Outline each blood parasite and name the species.
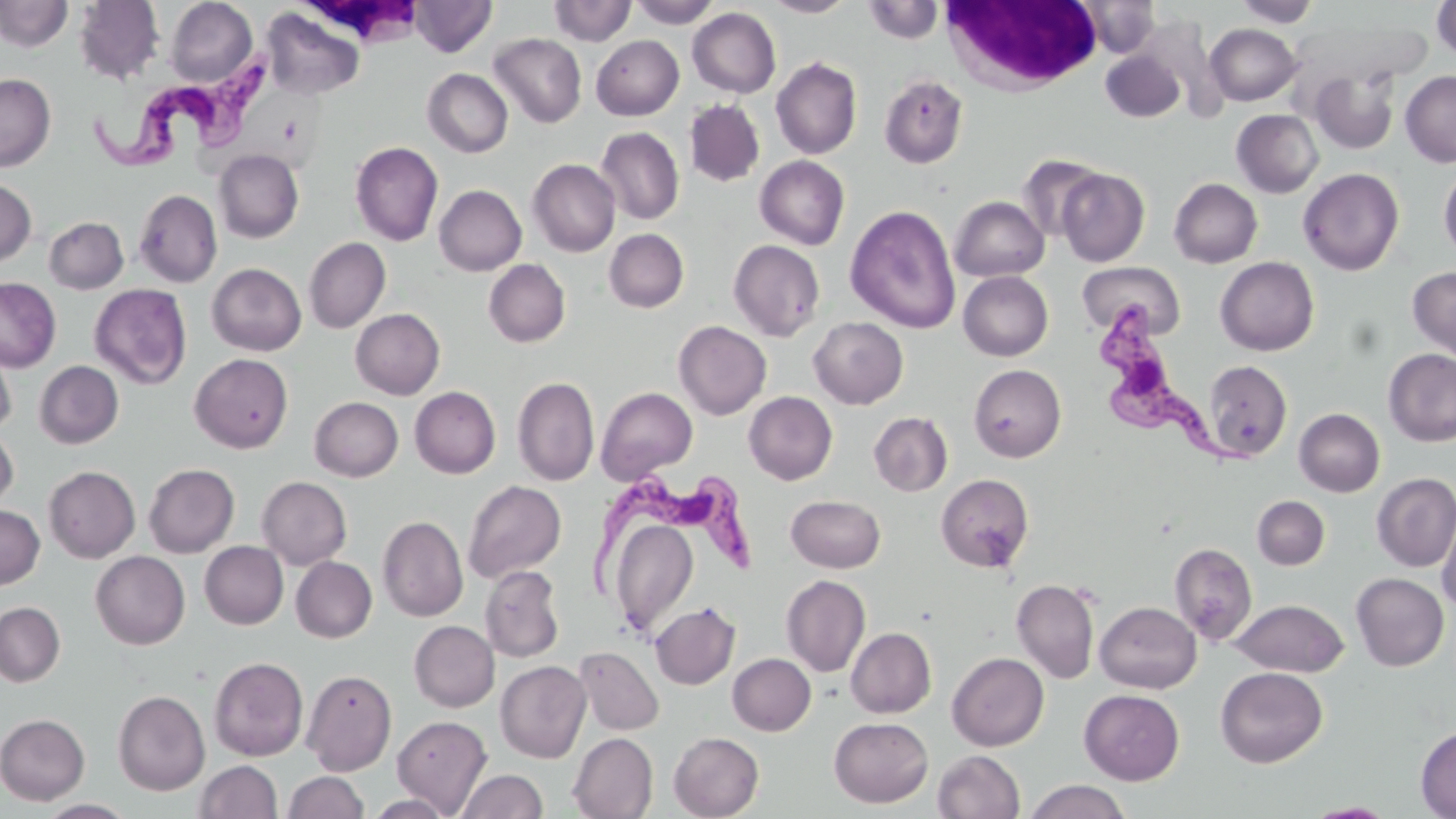

Approximate bounding boxes as named x1/y1/x2/y2 corners in pixels.
Trypanosoma brucei: (x1=91, y1=58, x2=277, y2=172), (x1=1099, y1=305, x2=1256, y2=478), (x1=589, y1=474, x2=756, y2=607).
No Plasmodium falciparum, Plasmodium ovale, Plasmodium malariae, Plasmodium vivax, or Babesia divergens observed.

Summary:
  - White blood cell locations: (x1=299, y1=0, x2=428, y2=50), (x1=941, y1=0, x2=1104, y2=95)
  - Uninfected red blood cell locations: (x1=0, y1=0, x2=72, y2=51), (x1=74, y1=0, x2=164, y2=84), (x1=165, y1=0, x2=257, y2=86), (x1=410, y1=0, x2=496, y2=57), (x1=549, y1=0, x2=636, y2=46), (x1=628, y1=0, x2=721, y2=28), (x1=763, y1=0, x2=857, y2=17), (x1=1077, y1=0, x2=1162, y2=58), (x1=1235, y1=0, x2=1321, y2=28), (x1=1432, y1=0, x2=1456, y2=62), (x1=863, y1=1, x2=943, y2=43), (x1=688, y1=7, x2=781, y2=97), (x1=261, y1=8, x2=364, y2=100), (x1=1133, y1=17, x2=1226, y2=117), (x1=1205, y1=23, x2=1302, y2=105), (x1=489, y1=33, x2=586, y2=128), (x1=591, y1=35, x2=683, y2=120), (x1=1101, y1=50, x2=1184, y2=122), (x1=771, y1=57, x2=862, y2=159), (x1=422, y1=68, x2=512, y2=158), (x1=1307, y1=68, x2=1399, y2=153), (x1=1400, y1=71, x2=1456, y2=166), (x1=0, y1=73, x2=56, y2=172), (x1=879, y1=75, x2=968, y2=168), (x1=684, y1=100, x2=764, y2=187), (x1=1231, y1=109, x2=1323, y2=198), (x1=596, y1=127, x2=684, y2=225), (x1=350, y1=141, x2=443, y2=246), (x1=214, y1=149, x2=304, y2=243), (x1=1017, y1=155, x2=1106, y2=242), (x1=755, y1=156, x2=849, y2=249), (x1=528, y1=159, x2=620, y2=257), (x1=1298, y1=167, x2=1404, y2=276), (x1=1439, y1=167, x2=1456, y2=260), (x1=1056, y1=168, x2=1149, y2=267), (x1=1169, y1=178, x2=1262, y2=268), (x1=0, y1=179, x2=37, y2=265), (x1=434, y1=185, x2=526, y2=276), (x1=134, y1=189, x2=222, y2=287), (x1=950, y1=196, x2=1049, y2=281), (x1=845, y1=205, x2=961, y2=334), (x1=44, y1=216, x2=128, y2=294), (x1=604, y1=229, x2=689, y2=312), (x1=304, y1=237, x2=391, y2=333), (x1=728, y1=239, x2=825, y2=341), (x1=1215, y1=256, x2=1319, y2=356), (x1=483, y1=259, x2=570, y2=348), (x1=1077, y1=261, x2=1185, y2=338), (x1=207, y1=263, x2=306, y2=355), (x1=1407, y1=266, x2=1456, y2=361), (x1=958, y1=271, x2=1053, y2=360), (x1=0, y1=277, x2=61, y2=372), (x1=90, y1=283, x2=192, y2=389), (x1=350, y1=308, x2=445, y2=399), (x1=809, y1=316, x2=908, y2=408), (x1=673, y1=321, x2=771, y2=419), (x1=0, y1=337, x2=17, y2=434), (x1=1383, y1=349, x2=1456, y2=446), (x1=190, y1=353, x2=293, y2=452), (x1=1203, y1=360, x2=1292, y2=461), (x1=35, y1=361, x2=123, y2=449), (x1=969, y1=364, x2=1065, y2=462), (x1=513, y1=376, x2=599, y2=486), (x1=409, y1=386, x2=500, y2=479), (x1=596, y1=386, x2=698, y2=483), (x1=743, y1=391, x2=837, y2=484), (x1=309, y1=396, x2=403, y2=481), (x1=1294, y1=408, x2=1385, y2=497), (x1=869, y1=412, x2=952, y2=496), (x1=0, y1=425, x2=18, y2=512), (x1=143, y1=463, x2=239, y2=557), (x1=44, y1=466, x2=140, y2=563), (x1=1364, y1=472, x2=1451, y2=671), (x1=1372, y1=472, x2=1456, y2=572), (x1=935, y1=473, x2=1034, y2=573), (x1=257, y1=476, x2=352, y2=569), (x1=463, y1=480, x2=566, y2=583), (x1=786, y1=495, x2=886, y2=573), (x1=1252, y1=495, x2=1330, y2=570), (x1=1437, y1=502, x2=1456, y2=615), (x1=0, y1=504, x2=44, y2=589), (x1=605, y1=510, x2=702, y2=640), (x1=378, y1=515, x2=468, y2=621), (x1=199, y1=541, x2=288, y2=629), (x1=1169, y1=543, x2=1257, y2=644), (x1=91, y1=551, x2=190, y2=649), (x1=291, y1=556, x2=377, y2=642), (x1=481, y1=565, x2=564, y2=663), (x1=1351, y1=573, x2=1449, y2=671), (x1=781, y1=575, x2=871, y2=677), (x1=1012, y1=578, x2=1100, y2=684), (x1=1229, y1=598, x2=1348, y2=677), (x1=0, y1=601, x2=65, y2=686), (x1=1095, y1=601, x2=1202, y2=693), (x1=650, y1=602, x2=740, y2=689), (x1=409, y1=620, x2=499, y2=712), (x1=846, y1=627, x2=936, y2=717), (x1=574, y1=646, x2=664, y2=736), (x1=947, y1=652, x2=1049, y2=750), (x1=728, y1=653, x2=816, y2=735), (x1=209, y1=656, x2=308, y2=761), (x1=495, y1=660, x2=591, y2=763), (x1=1215, y1=666, x2=1328, y2=767), (x1=302, y1=669, x2=396, y2=775), (x1=113, y1=689, x2=210, y2=795), (x1=1079, y1=689, x2=1184, y2=785), (x1=0, y1=713, x2=90, y2=804), (x1=392, y1=715, x2=492, y2=815), (x1=829, y1=716, x2=933, y2=807), (x1=1415, y1=725, x2=1456, y2=818), (x1=568, y1=732, x2=657, y2=819), (x1=669, y1=732, x2=764, y2=818), (x1=933, y1=750, x2=1025, y2=819), (x1=195, y1=760, x2=283, y2=818), (x1=456, y1=769, x2=547, y2=818), (x1=283, y1=771, x2=369, y2=819), (x1=1023, y1=780, x2=1132, y2=819), (x1=364, y1=794, x2=456, y2=818), (x1=35, y1=799, x2=137, y2=818)
  - Slide-level diagnosis: Trypanosoma brucei
  - Image size: 1456×819 pixels
  - Magnification: 1000x
  - Field of view: one of a larger specimen
  - Stain: May-Grünwald-Giemsa
  - Preparation: thin blood film
  - Modality: light microscopy